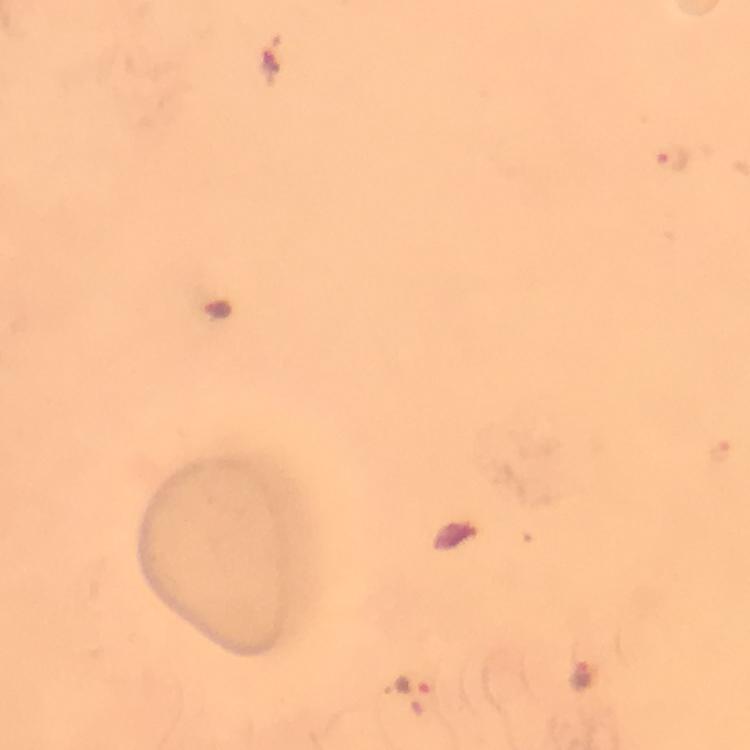
Approximate centers as {x, y} in pixels. Malaria parasite locations: {674, 157}, {721, 447}, {582, 677}, {411, 686}. 100x magnification. From a diagnostic examination for malaria. Giemsa stain. Photographed through the microscope with a smartphone camera. Cropped region of a single field of view. Thick smear. Image is 750×750 pixels. Immersion oil was used.